Name the blood parasite species.
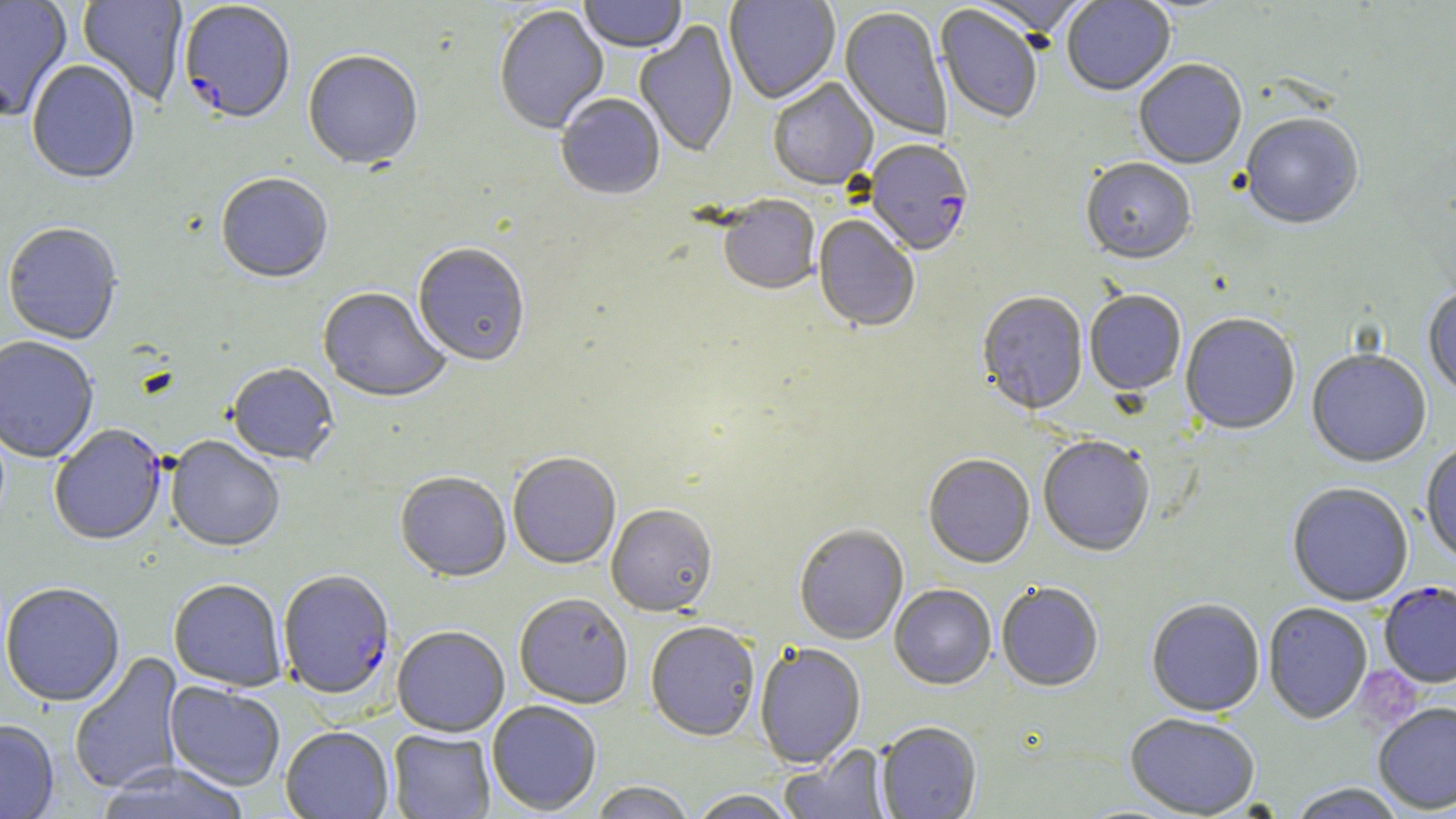

Plasmodium falciparum.

preparation = thin blood smear
uninfected red blood cell locations = approximate bounding boxes as named x1/y1/x2/y2 corners in pixels: (x1=0, y1=0, x2=72, y2=121), (x1=77, y1=0, x2=189, y2=106), (x1=579, y1=0, x2=687, y2=54), (x1=724, y1=0, x2=840, y2=105), (x1=971, y1=0, x2=1094, y2=40), (x1=1062, y1=0, x2=1176, y2=98), (x1=934, y1=5, x2=1042, y2=125), (x1=494, y1=6, x2=609, y2=137), (x1=840, y1=8, x2=951, y2=141), (x1=634, y1=21, x2=738, y2=159), (x1=303, y1=53, x2=423, y2=173), (x1=1134, y1=61, x2=1248, y2=171), (x1=26, y1=62, x2=140, y2=187), (x1=768, y1=79, x2=879, y2=192), (x1=556, y1=95, x2=666, y2=202), (x1=1240, y1=115, x2=1364, y2=232), (x1=1081, y1=161, x2=1196, y2=267), (x1=216, y1=175, x2=333, y2=285), (x1=718, y1=197, x2=820, y2=297), (x1=813, y1=216, x2=919, y2=334), (x1=2, y1=223, x2=123, y2=346), (x1=413, y1=245, x2=530, y2=368), (x1=318, y1=289, x2=450, y2=405), (x1=1423, y1=289, x2=1456, y2=399), (x1=1084, y1=292, x2=1186, y2=397), (x1=977, y1=293, x2=1089, y2=417), (x1=1180, y1=315, x2=1300, y2=437), (x1=0, y1=337, x2=99, y2=464), (x1=1307, y1=351, x2=1431, y2=469), (x1=226, y1=365, x2=339, y2=468), (x1=166, y1=437, x2=284, y2=554), (x1=1038, y1=437, x2=1155, y2=558), (x1=1420, y1=443, x2=1456, y2=566), (x1=507, y1=455, x2=621, y2=570), (x1=923, y1=456, x2=1035, y2=570), (x1=395, y1=474, x2=511, y2=584), (x1=1287, y1=484, x2=1413, y2=608), (x1=606, y1=505, x2=718, y2=618), (x1=794, y1=526, x2=909, y2=646), (x1=169, y1=581, x2=287, y2=692), (x1=0, y1=584, x2=125, y2=708), (x1=996, y1=584, x2=1103, y2=693), (x1=889, y1=585, x2=996, y2=691), (x1=514, y1=595, x2=633, y2=709), (x1=1146, y1=600, x2=1265, y2=718), (x1=1263, y1=604, x2=1373, y2=725), (x1=645, y1=622, x2=760, y2=743), (x1=393, y1=627, x2=509, y2=738), (x1=754, y1=643, x2=866, y2=770), (x1=69, y1=651, x2=185, y2=795), (x1=165, y1=682, x2=286, y2=791), (x1=487, y1=701, x2=602, y2=815), (x1=1373, y1=704, x2=1456, y2=815), (x1=1125, y1=715, x2=1261, y2=818), (x1=0, y1=719, x2=59, y2=819), (x1=876, y1=723, x2=982, y2=819), (x1=280, y1=727, x2=394, y2=819), (x1=388, y1=729, x2=495, y2=818), (x1=779, y1=744, x2=894, y2=818), (x1=96, y1=761, x2=250, y2=819), (x1=589, y1=782, x2=695, y2=819), (x1=1288, y1=784, x2=1407, y2=819), (x1=688, y1=790, x2=801, y2=819)
stain = May-Grünwald-Giemsa
magnification = 1000x
Plasmodium falciparum-infected red blood cell locations = approximate bounding boxes as named x1/y1/x2/y2 corners in pixels: (x1=179, y1=3, x2=296, y2=128), (x1=864, y1=141, x2=974, y2=259), (x1=49, y1=424, x2=167, y2=547), (x1=278, y1=571, x2=395, y2=702), (x1=1379, y1=583, x2=1456, y2=688)
platelet locations = approximate bounding boxes as named x1/y1/x2/y2 corners in pixels: (x1=1356, y1=667, x2=1423, y2=730)
image size = 1456×819 pixels
field of view = single
modality = optical microscopy